Point out every Plasmodium parasite.
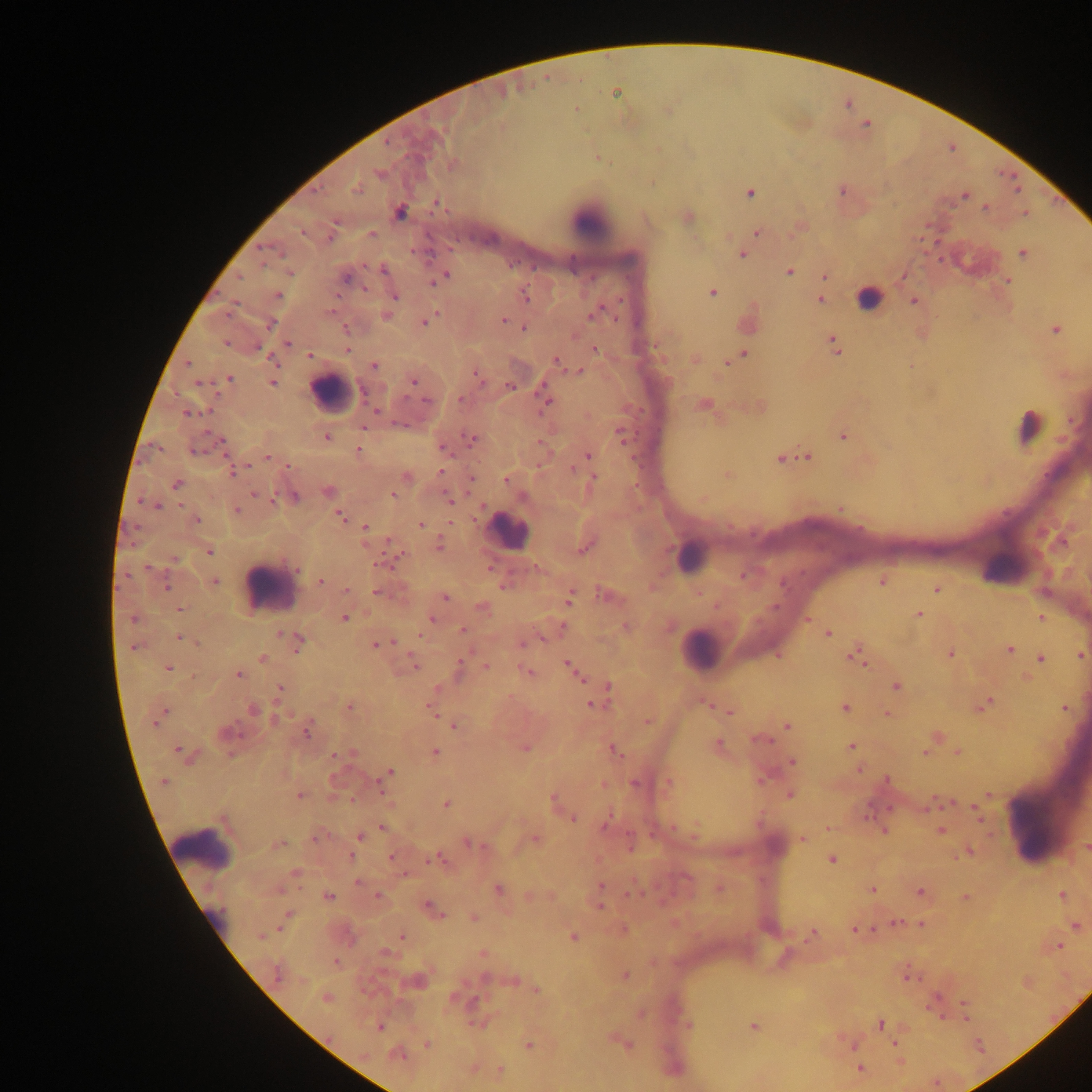
Approximate centers as {x, y} in pixels.
Plasmodium parasites: {616, 92}, {576, 109}, {599, 158}, {453, 165}, {357, 190}, {842, 191}, {750, 193}, {965, 196}, {437, 203}, {987, 207}, {400, 212}, {1025, 213}, {302, 232}, {758, 232}, {371, 234}, {330, 237}, {742, 254}, {1023, 254}, {383, 270}, {789, 272}, {289, 273}, {445, 276}, {239, 277}, {825, 277}, {346, 279}, {439, 280}, {1007, 281}, {364, 289}, {712, 292}, {278, 295}, {395, 296}, {526, 297}, {820, 300}, {914, 301}, {595, 313}, {386, 316}, {432, 317}, {504, 320}, {425, 322}, {270, 324}, {524, 327}, {346, 329}, {1056, 330}, {225, 343}, {288, 343}, {833, 345}, {595, 349}, {348, 350}, {743, 354}, {310, 355}, {268, 356}, {735, 358}, {557, 362}, {188, 364}, {374, 365}, {580, 371}, {229, 378}, {478, 378}, {413, 381}, {199, 383}, {272, 383}, {509, 386}, {364, 392}, {459, 399}, {546, 401}, {426, 402}, {376, 410}, {188, 414}, {400, 424}, {363, 428}, {620, 433}, {327, 437}, {843, 437}, {472, 438}, {220, 441}, {443, 448}, {358, 450}, {194, 451}, {588, 456}, {268, 457}, {808, 457}, {781, 459}, {289, 466}, {247, 467}, {573, 469}, {232, 472}, {441, 472}, {727, 475}, {593, 477}, {471, 478}, {506, 479}, {176, 484}, {328, 491}, {254, 494}, {392, 495}, {523, 497}, {294, 498}, {277, 499}, {449, 499}, {156, 506}, {841, 509}, {236, 511}, {340, 515}, {196, 520}, {420, 525}, {366, 527}, {439, 546}, {584, 548}, {209, 552}, {175, 560}, {381, 564}, {147, 568}, {742, 576}, {214, 581}, {320, 581}, {882, 581}, {166, 587}, {503, 587}, {937, 589}, {346, 590}, {376, 592}, {444, 597}, {570, 599}, {483, 608}, {180, 609}, {919, 614}, {1041, 617}, {345, 618}, {133, 619}, {431, 620}, {808, 620}, {462, 630}, {280, 634}, {828, 634}, {421, 635}, {180, 638}, {297, 640}, {196, 642}, {390, 642}, {383, 643}, {523, 643}, {376, 644}, {134, 648}, {1010, 649}, {950, 654}, {855, 655}, {1080, 655}, {263, 658}, {1041, 659}, {413, 663}, {569, 664}, {459, 667}, {486, 667}, {168, 668}, {528, 672}, {577, 674}, {238, 675}, {897, 687}, {280, 688}, {609, 688}, {705, 703}, {593, 704}, {985, 704}, {349, 706}, {431, 707}, {845, 708}, {1065, 709}, {253, 710}, {729, 712}, {162, 714}, {888, 714}, {278, 717}, {156, 721}, {647, 722}, {454, 725}, {787, 726}, {307, 732}, {760, 740}, {718, 744}, {851, 746}, {525, 748}, {180, 751}, {436, 752}, {616, 752}, {924, 752}, {957, 752}, {351, 753}, {335, 756}, {792, 763}, {859, 770}, {390, 772}, {886, 780}, {163, 782}, {635, 784}, {669, 784}, {603, 785}, {789, 794}, {299, 796}, {553, 799}, {446, 805}, {976, 807}, {978, 814}, {573, 819}, {606, 824}, {382, 827}, {828, 828}, {885, 830}, {941, 831}, {361, 837}, {318, 838}, {802, 839}, {535, 840}, {469, 843}, {279, 844}, {1086, 847}, {969, 852}, {350, 856}, {392, 857}, {435, 859}, {832, 860}, {295, 872}, {406, 874}, {358, 881}, {601, 886}, {719, 888}, {498, 889}, {873, 889}, {920, 892}, {378, 895}, {1062, 895}, {328, 896}, {965, 897}, {429, 906}, {600, 907}, {436, 911}, {440, 915}, {474, 917}, {286, 918}, {897, 922}, {921, 925}, {1076, 926}, {855, 930}, {812, 935}, {261, 936}, {401, 936}, {573, 936}, {1058, 946}, {483, 954}, {336, 962}, {276, 973}, {625, 976}, {910, 977}, {536, 990}, {325, 997}, {935, 997}, {965, 1005}, {966, 1017}, {688, 1025}, {880, 1025}, {754, 1027}, {380, 1028}, {529, 1044}, {851, 1044}, {895, 1044}, {427, 1045}, {627, 1045}, {398, 1055}, {860, 1069}, {500, 1070}.

{
  "preparation": "thick blood smear",
  "country": "Ghana",
  "image_size": "1092×1092 pixels",
  "capture": "mobile-phone photograph through a microscope",
  "leukocyte_locations": "approximate centers as {x, y} in pixels: {591, 221}, {868, 298}, {331, 391}, {1032, 425}, {508, 531}, {691, 555}, {1006, 567}, {272, 586}, {700, 649}, {1029, 825}, {203, 848}, {213, 915}",
  "field_of_view": "single"
}